State which parasite is depicted.
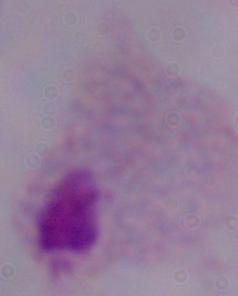

A trichomonad.

magnification = 1000x
modality = micrograph